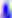
identification = Toxoplasma gondii
modality = photomicrograph
magnification = 400x